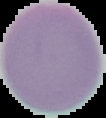

Image is 106×118 pixels. The area outside the segmented cell region is set to black. Result: no malaria parasites detected. From a thin blood film.